Locate every blood parasite and identify its species.
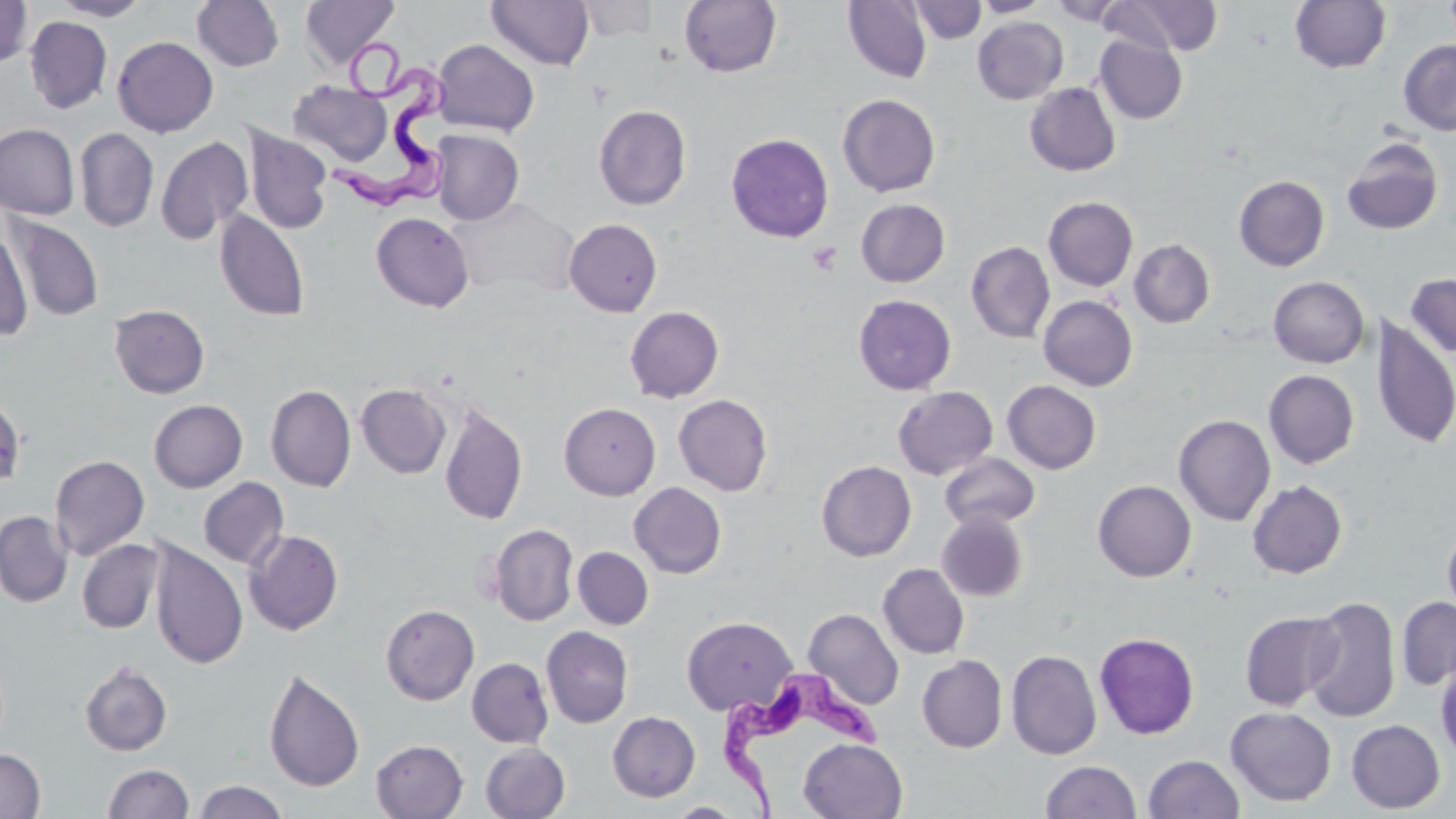
Approximate bounding boxes as named x1/y1/x2/y2 corners in pixels.
Trypanosoma brucei: (x1=324, y1=23, x2=460, y2=214), (x1=723, y1=668, x2=889, y2=819).
No Plasmodium falciparum, Plasmodium ovale, Plasmodium malariae, Plasmodium vivax, or Babesia divergens observed.

Platelet locations: (x1=807, y1=242, x2=843, y2=276). Uninfected red blood cell locations: (x1=0, y1=0, x2=33, y2=69), (x1=50, y1=0, x2=152, y2=20), (x1=300, y1=0, x2=400, y2=71), (x1=486, y1=0, x2=594, y2=71), (x1=842, y1=0, x2=933, y2=83), (x1=972, y1=0, x2=1051, y2=17), (x1=1048, y1=0, x2=1131, y2=26), (x1=1102, y1=0, x2=1224, y2=56), (x1=1289, y1=0, x2=1391, y2=74), (x1=191, y1=1, x2=285, y2=72), (x1=574, y1=1, x2=662, y2=42), (x1=679, y1=1, x2=782, y2=77), (x1=909, y1=1, x2=987, y2=44), (x1=25, y1=16, x2=113, y2=114), (x1=973, y1=16, x2=1068, y2=104), (x1=1094, y1=34, x2=1188, y2=124), (x1=112, y1=36, x2=218, y2=137), (x1=433, y1=39, x2=540, y2=136), (x1=1397, y1=40, x2=1456, y2=135), (x1=289, y1=81, x2=393, y2=166), (x1=1024, y1=83, x2=1121, y2=176), (x1=837, y1=93, x2=941, y2=197), (x1=593, y1=104, x2=691, y2=210), (x1=0, y1=123, x2=80, y2=220), (x1=242, y1=125, x2=333, y2=235), (x1=75, y1=128, x2=159, y2=232), (x1=431, y1=129, x2=524, y2=225), (x1=726, y1=133, x2=834, y2=242), (x1=155, y1=136, x2=254, y2=245), (x1=1341, y1=137, x2=1444, y2=235), (x1=1233, y1=175, x2=1329, y2=271), (x1=1043, y1=196, x2=1138, y2=291), (x1=450, y1=198, x2=578, y2=299), (x1=856, y1=199, x2=950, y2=287), (x1=214, y1=210, x2=310, y2=322), (x1=371, y1=211, x2=474, y2=312), (x1=7, y1=215, x2=105, y2=322), (x1=564, y1=219, x2=662, y2=317), (x1=0, y1=227, x2=34, y2=340), (x1=1129, y1=239, x2=1215, y2=328), (x1=966, y1=242, x2=1055, y2=343), (x1=1405, y1=272, x2=1456, y2=358), (x1=1268, y1=276, x2=1369, y2=368), (x1=853, y1=294, x2=957, y2=395), (x1=1038, y1=295, x2=1138, y2=391), (x1=109, y1=304, x2=210, y2=399), (x1=624, y1=306, x2=724, y2=403), (x1=1372, y1=317, x2=1455, y2=449), (x1=1264, y1=369, x2=1359, y2=469), (x1=1002, y1=380, x2=1101, y2=474), (x1=356, y1=383, x2=451, y2=478), (x1=265, y1=384, x2=356, y2=492), (x1=893, y1=386, x2=998, y2=480), (x1=0, y1=393, x2=26, y2=493), (x1=673, y1=394, x2=773, y2=496), (x1=149, y1=399, x2=247, y2=493), (x1=559, y1=402, x2=660, y2=500), (x1=439, y1=404, x2=528, y2=525), (x1=1173, y1=414, x2=1276, y2=526), (x1=940, y1=453, x2=1040, y2=531), (x1=49, y1=455, x2=150, y2=561), (x1=817, y1=461, x2=916, y2=561), (x1=198, y1=477, x2=289, y2=569), (x1=1092, y1=480, x2=1196, y2=582), (x1=1247, y1=480, x2=1347, y2=579), (x1=629, y1=483, x2=727, y2=578), (x1=0, y1=511, x2=72, y2=607), (x1=937, y1=512, x2=1029, y2=602), (x1=1442, y1=521, x2=1456, y2=623), (x1=489, y1=524, x2=579, y2=626), (x1=244, y1=529, x2=344, y2=636), (x1=76, y1=539, x2=163, y2=634), (x1=148, y1=541, x2=248, y2=669), (x1=572, y1=546, x2=653, y2=629), (x1=878, y1=564, x2=969, y2=659), (x1=1302, y1=596, x2=1401, y2=723), (x1=1396, y1=596, x2=1456, y2=690), (x1=380, y1=604, x2=479, y2=705), (x1=803, y1=608, x2=904, y2=710), (x1=1240, y1=611, x2=1343, y2=711), (x1=681, y1=616, x2=798, y2=715), (x1=541, y1=626, x2=634, y2=728), (x1=1094, y1=632, x2=1199, y2=739), (x1=1006, y1=650, x2=1102, y2=760), (x1=917, y1=655, x2=1007, y2=753), (x1=467, y1=658, x2=553, y2=748), (x1=79, y1=660, x2=173, y2=756), (x1=1436, y1=660, x2=1456, y2=761), (x1=263, y1=668, x2=365, y2=792), (x1=1225, y1=705, x2=1337, y2=807), (x1=607, y1=711, x2=701, y2=803), (x1=1346, y1=719, x2=1445, y2=813), (x1=799, y1=738, x2=908, y2=819), (x1=371, y1=739, x2=468, y2=819), (x1=480, y1=742, x2=570, y2=819), (x1=0, y1=749, x2=46, y2=818), (x1=1143, y1=754, x2=1244, y2=818), (x1=1040, y1=760, x2=1142, y2=819), (x1=103, y1=763, x2=194, y2=819), (x1=193, y1=780, x2=289, y2=819), (x1=667, y1=802, x2=745, y2=818). Slide-level diagnosis: Trypanosoma brucei. Single field of view. May-Grünwald-Giemsa-stained preparation. Image is 1456×819 pixels. Optical microscopy. Thin blood film. Captured at 1000x magnification.